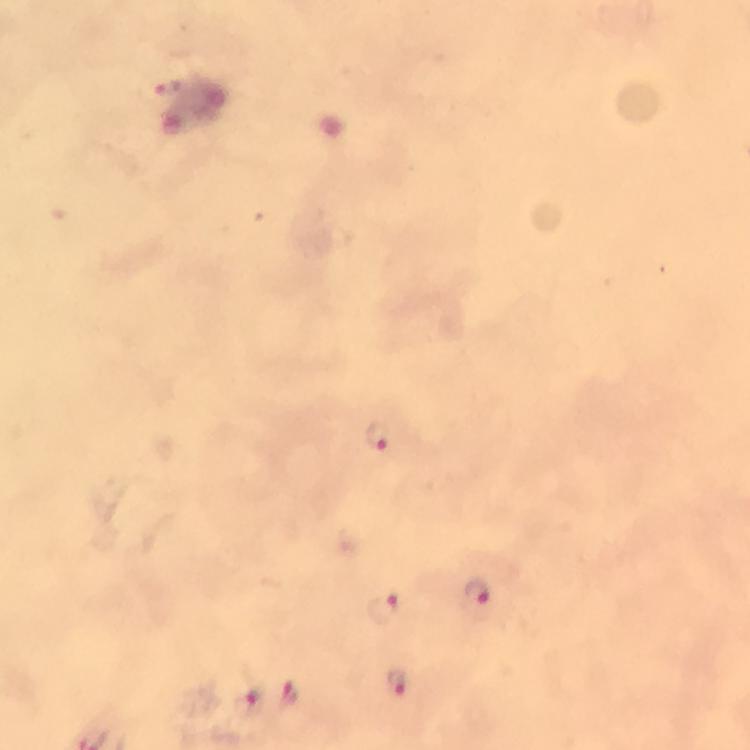

Approximate object centers, in pixels from the top-left corner.
Summary:
  - Malaria parasite locations: (x=167, y=88), (x=379, y=436), (x=477, y=590), (x=385, y=607), (x=398, y=684), (x=286, y=694), (x=246, y=700)
  - Immersion oil: applied
  - Context: from a malaria diagnostic workup
  - Preparation: thick blood smear
  - Magnification: 100x
  - Stain: Giemsa
  - Image size: 750×750 pixels
  - Cropped from: a single field of view
  - Capture: smartphone photograph through a microscope